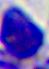
Summary:
  - Modality: micrograph
  - Identification: white blood cell
  - Magnification: 400x